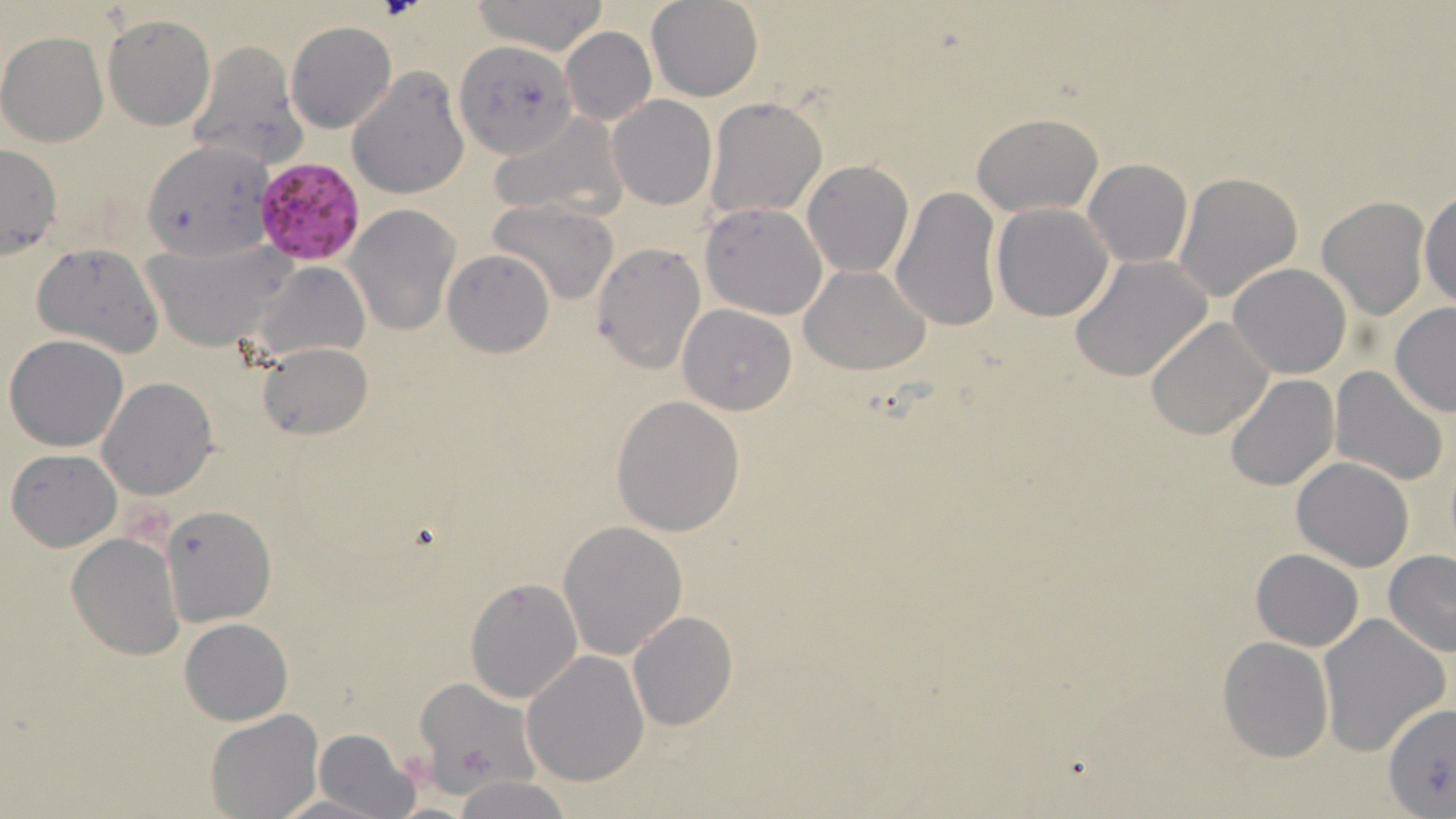

{
  "slide_level_diagnosis": "Plasmodium falciparum",
  "modality": "light microscopy",
  "field_of_view": "one of a larger specimen",
  "preparation": "thin blood smear",
  "uninfected_red_blood_cell_locations": "approximate bounding boxes as [x1, y1, x2, y2] in pixels: [468, 0, 610, 54], [647, 0, 762, 101], [104, 15, 215, 131], [286, 21, 396, 133], [559, 27, 656, 126], [0, 30, 110, 147], [186, 39, 306, 169], [454, 40, 580, 159], [347, 69, 470, 197], [607, 95, 717, 210], [703, 97, 828, 221], [490, 112, 625, 221], [973, 113, 1103, 218], [144, 141, 274, 260], [0, 145, 63, 259], [803, 160, 914, 277], [1083, 160, 1192, 268], [800, 170, 1002, 298], [1172, 172, 1303, 304], [891, 184, 1001, 331], [1418, 187, 1456, 310], [1317, 197, 1430, 320], [489, 200, 619, 306], [699, 202, 827, 320], [990, 202, 1114, 321], [345, 205, 460, 335], [143, 241, 297, 350], [31, 242, 165, 358], [591, 243, 705, 373], [442, 250, 553, 358], [1069, 255, 1213, 381], [253, 260, 370, 363], [1228, 263, 1352, 379], [799, 265, 932, 376], [1389, 302, 1456, 418], [678, 305, 797, 415], [1144, 316, 1276, 442], [5, 335, 130, 452], [258, 342, 371, 441], [1329, 366, 1451, 485], [1225, 375, 1338, 492], [98, 378, 218, 499], [611, 396, 744, 537], [6, 447, 122, 550], [1291, 457, 1414, 571], [160, 503, 276, 627], [558, 519, 688, 661], [67, 532, 185, 660], [1251, 548, 1363, 652], [1382, 550, 1456, 656], [465, 576, 583, 703], [627, 612, 737, 730], [1317, 613, 1450, 758], [179, 617, 293, 725], [1217, 637, 1335, 762], [522, 650, 650, 786], [414, 679, 537, 790], [1382, 699, 1455, 817], [206, 708, 322, 817], [313, 727, 422, 819], [453, 776, 575, 818], [269, 792, 394, 819]",
  "stain": "May-Grünwald-Giemsa",
  "plasmodium_falciparum_infected_red_blood_cell_locations": "approximate bounding boxes as [x1, y1, x2, y2] in pixels: [253, 158, 365, 265]",
  "magnification": "1000x",
  "image_size": "1456×819 pixels"
}